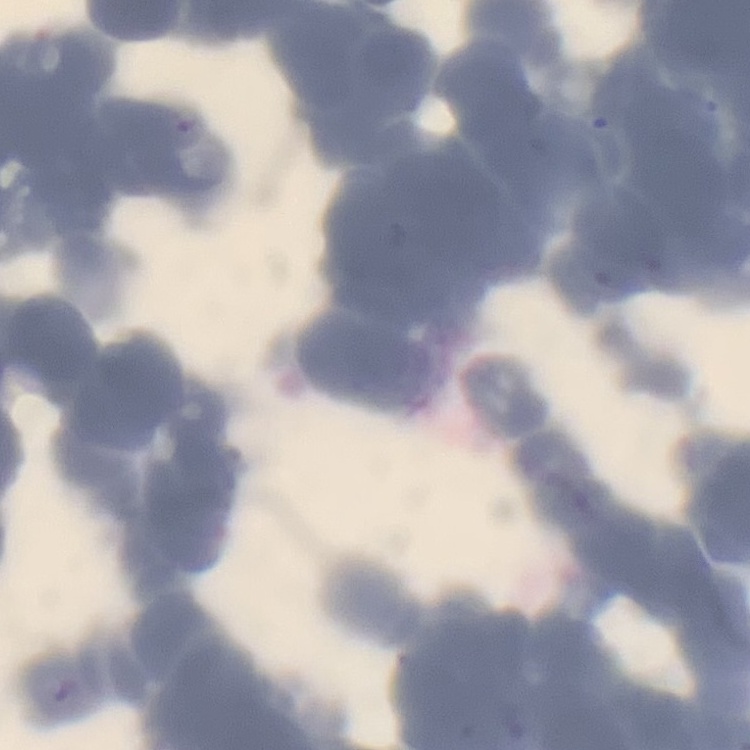
erythrocyte_morphology: rouleaux formation
preparation: thin peripheral smear
stain: Field's or Giemsa
image_type: square crop of a larger photomicrograph